Describe the morphology of the erythrocytes.
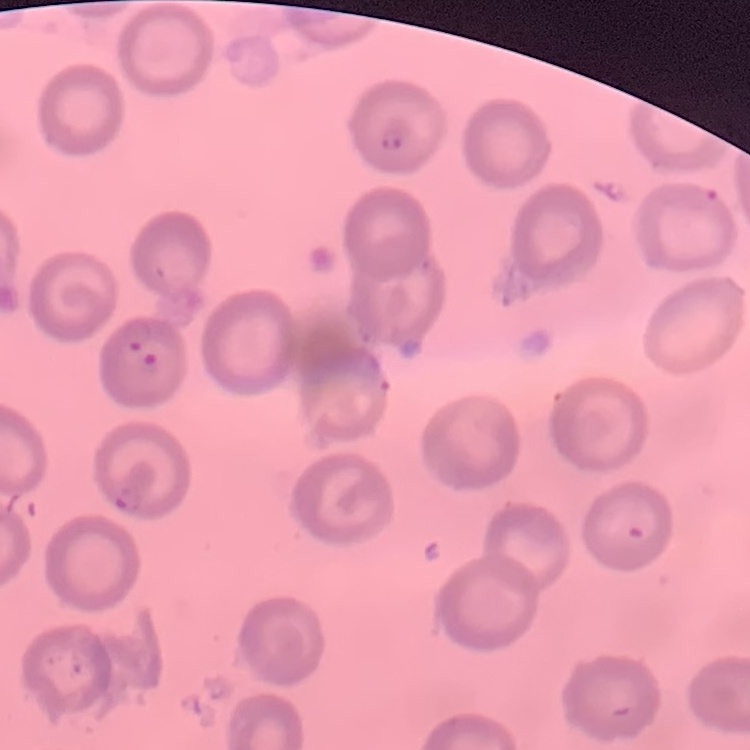
They show no rouleaux formation.

One tile cut from a larger photomicrograph. Thin blood smear. Stained with either Field's or Giemsa.